Assess the morphology of the erythrocytes.
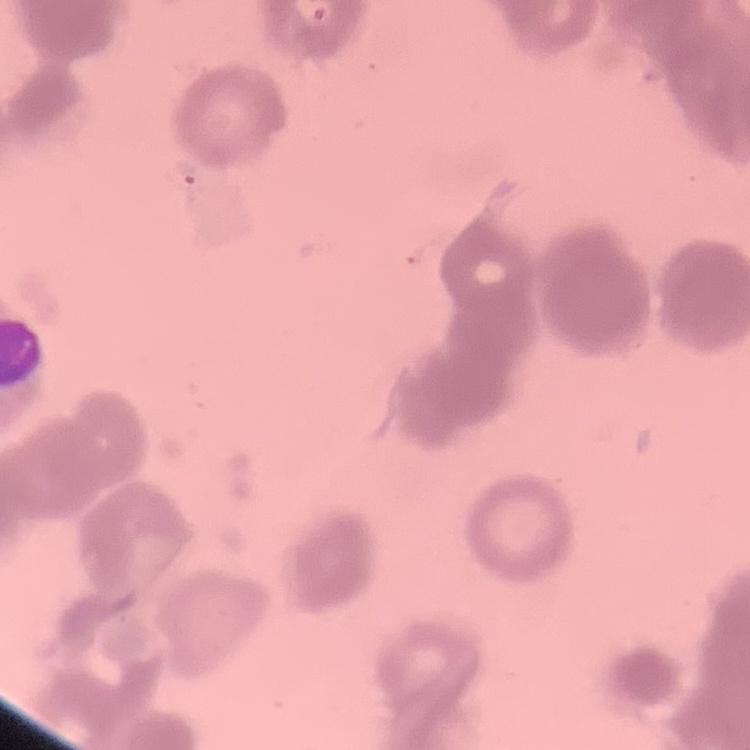
Rouleaux formation.

{
  "stain": "Field's or Giemsa",
  "preparation": "thin blood smear",
  "image_type": "square crop of a larger photomicrograph"
}